Identify the parasite.
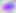

Toxoplasma gondii.

Summary:
  - Magnification: 400x
  - Modality: photomicrograph